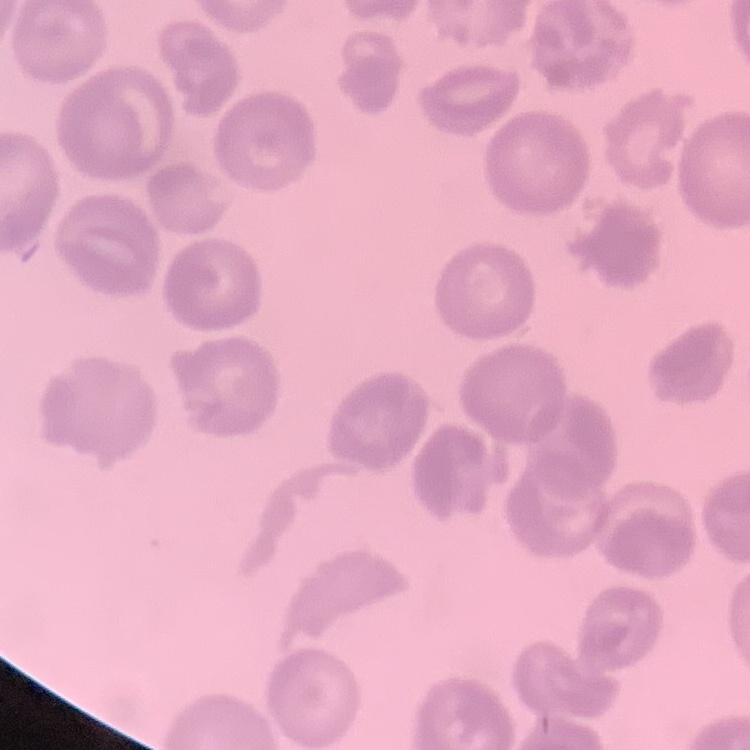
The erythrocytes show no rouleaux formation. Square crop of a larger photomicrograph. Thin peripheral smear. Field's or Giemsa stain.